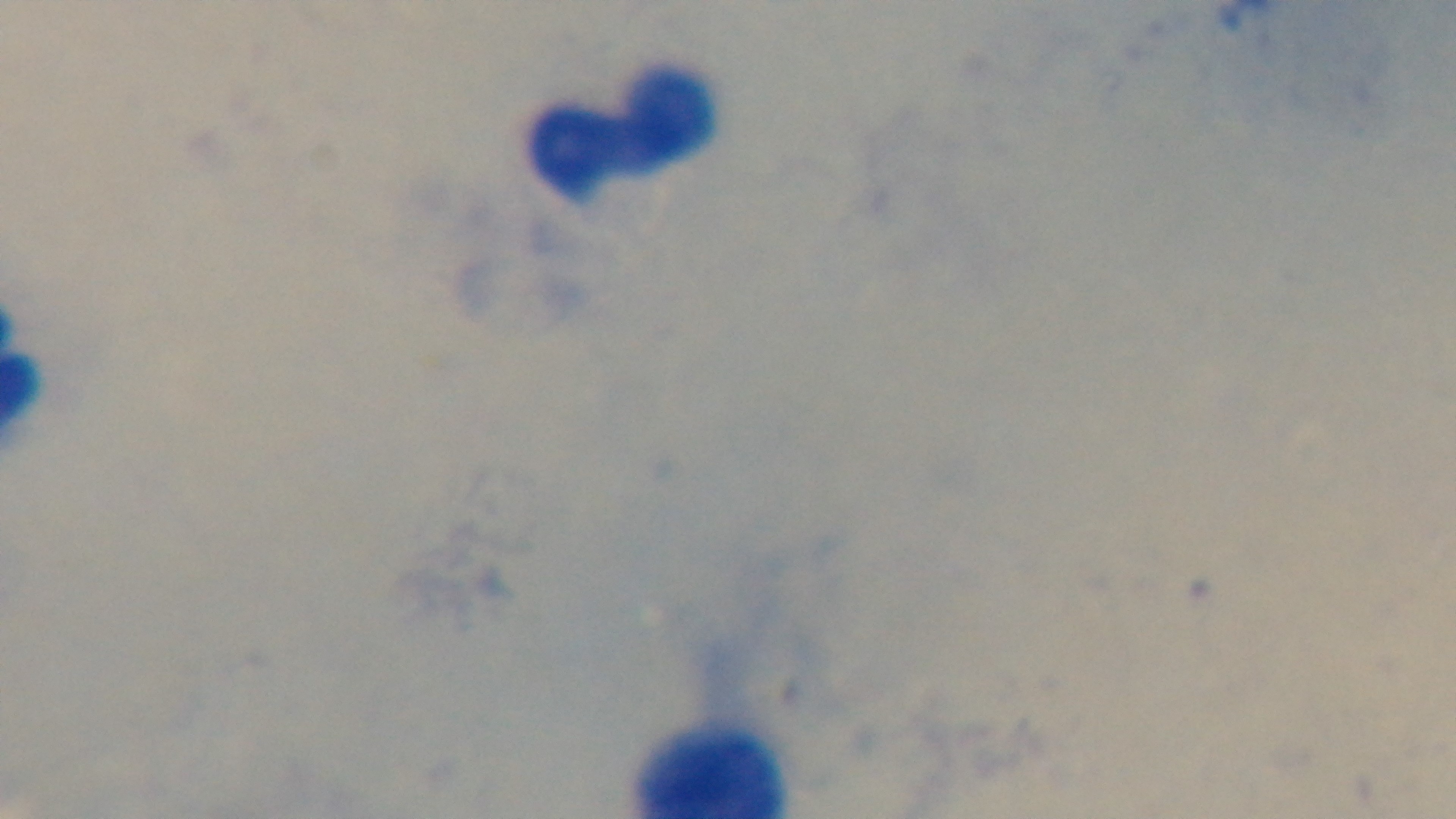
Summary:
  - Objective: 100x oil immersion
  - Malaria status: uninfected
  - Field of view: single
  - Preparation: thick
  - Stain: Giemsa
  - Capture: mounted 4K digital camera
  - Modality: light microscopy